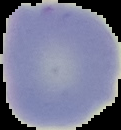
image_type: segmented cell region on a black background
preparation: thin blood film
image_size: 121×130 pixels
malaria_status: uninfected